Locate every malaria parasite and every leukocyte.
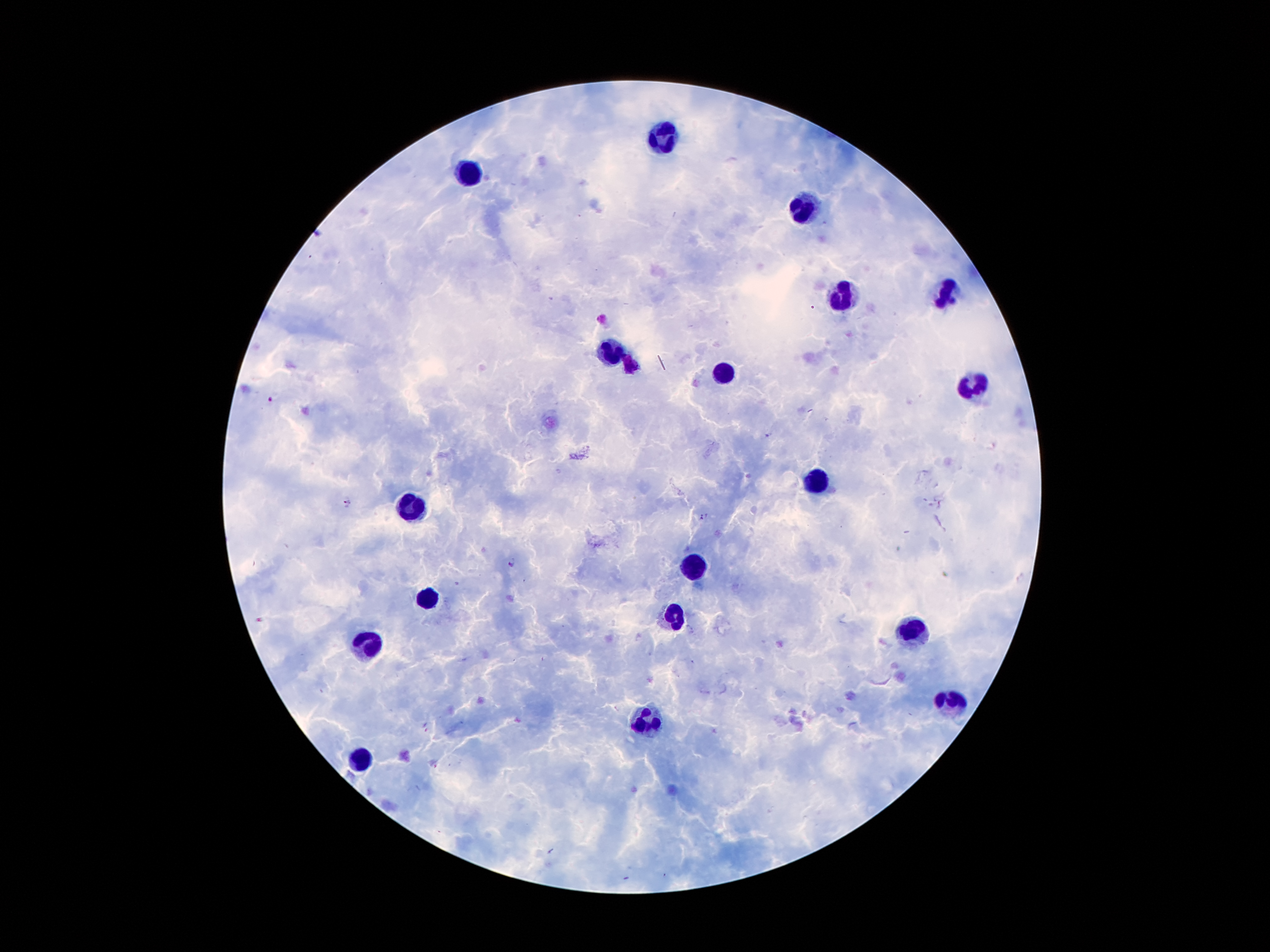

Approximate centers as {x, y} in pixels.
Malaria parasites: {270, 400}, {768, 436}, {347, 502}, {704, 518}, {512, 563}.
Leukocytes: {667, 139}, {468, 174}, {802, 214}, {945, 292}, {838, 298}, {613, 351}, {722, 374}, {974, 386}, {817, 485}, {413, 512}, {693, 567}, {428, 600}, {675, 619}, {916, 634}, {369, 648}, {952, 701}, {654, 722}, {362, 755}.

Thick peripheral-blood smear. Patient malaria status: positive for Plasmodium falciparum. Giemsa-stained preparation. Single field of view. Photographed through the microscope eyepiece with a smartphone camera. Image is 1270×952 pixels. 100x magnification.